Point out each Plasmodium parasite and each leukocyte.
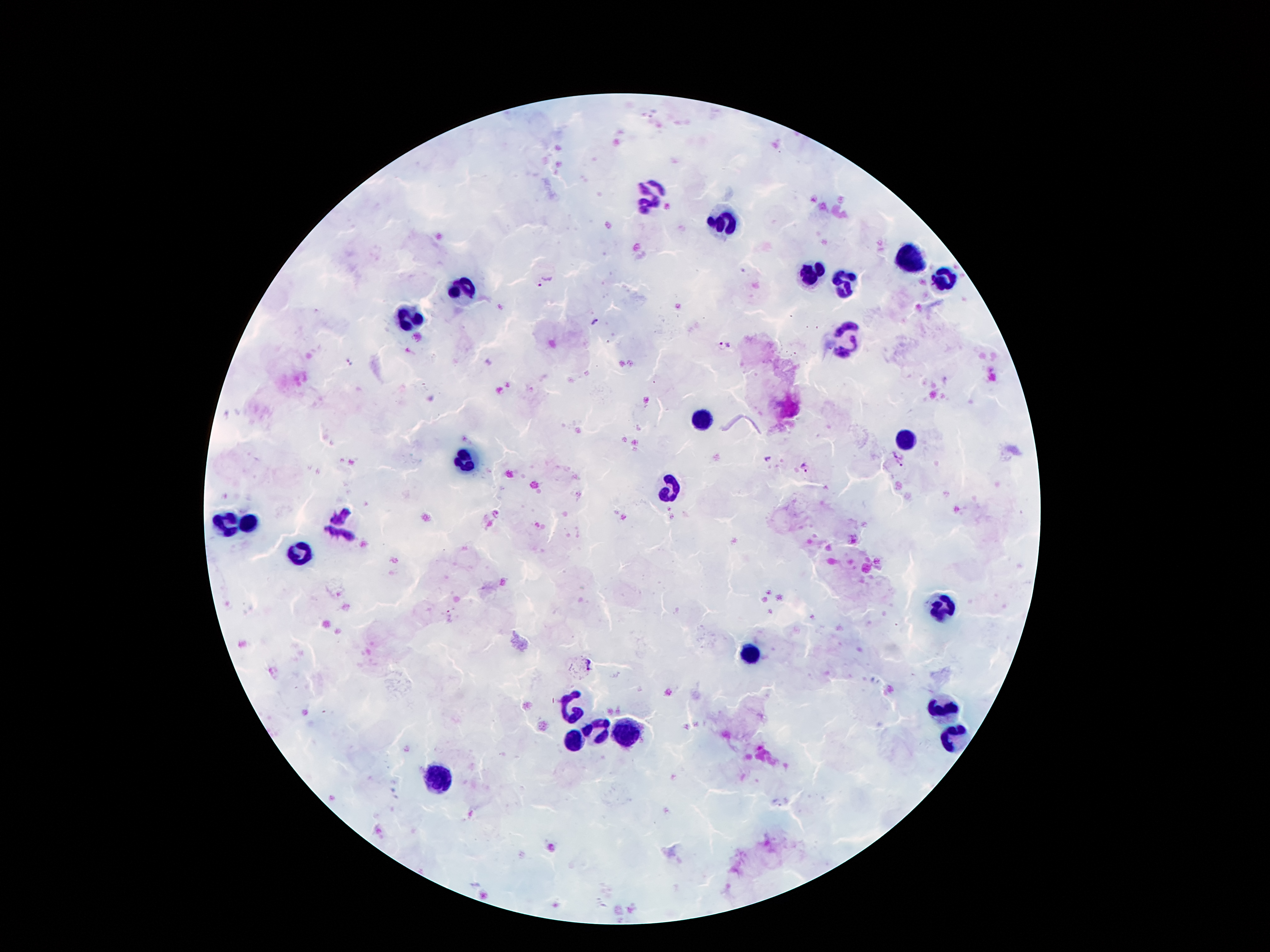

Approximate centers as [x, y] in pixels.
Plasmodium parasites: [547, 283], [597, 320], [724, 344], [347, 362], [897, 454], [769, 459], [899, 465], [805, 467], [449, 614], [588, 664].
Leukocytes: [652, 195], [727, 220], [910, 259], [813, 275], [942, 280], [845, 284], [461, 288], [409, 320], [842, 341], [697, 418], [910, 439], [463, 457], [668, 493], [225, 522], [248, 522], [338, 522], [300, 552], [942, 607], [749, 656], [942, 706], [570, 707], [597, 727], [627, 732], [572, 736], [952, 736], [434, 782].

Summary:
  - Field of view: one from this slide
  - Patient malaria status: positive for Plasmodium falciparum
  - Magnification: 100x
  - Capture: smartphone through the microscope eyepiece
  - Stain: Giemsa
  - Preparation: thick blood film
  - Image size: 1270×952 pixels